Classify this cell by malaria status.
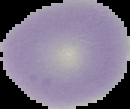

It is uninfected.

Summary:
  - Image type: segmented cell region with the area outside set to black
  - Preparation: thin blood smear
  - Image size: 130×109 pixels